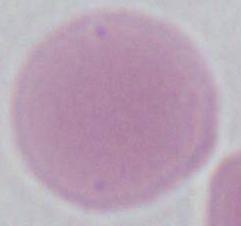
An erythrocyte is seen. Photomicrograph. 1000x magnification.